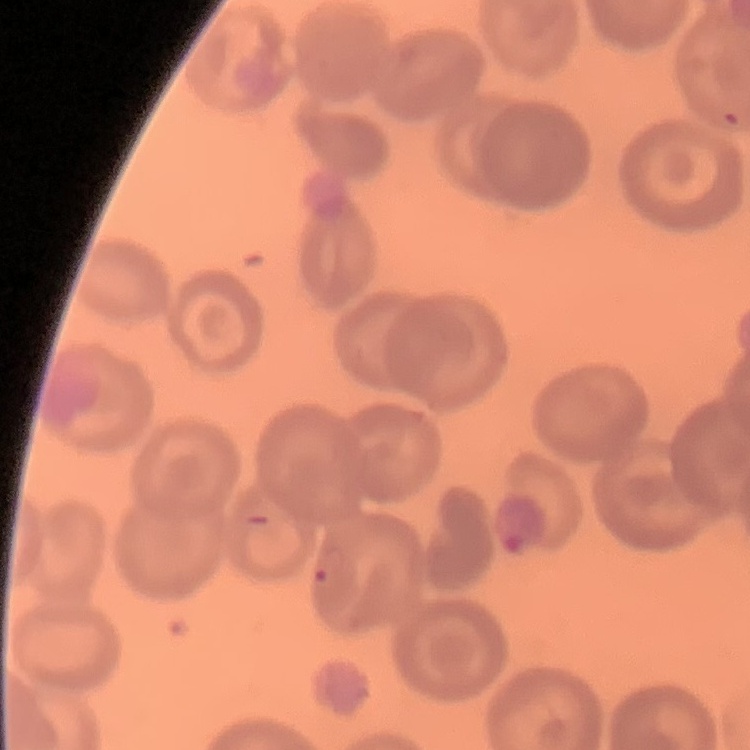

Summary:
  - Red blood cell morphology: no rouleaux formation
  - Stain: Field's or Giemsa
  - Preparation: thin blood smear
  - Image type: square crop of a larger photomicrograph